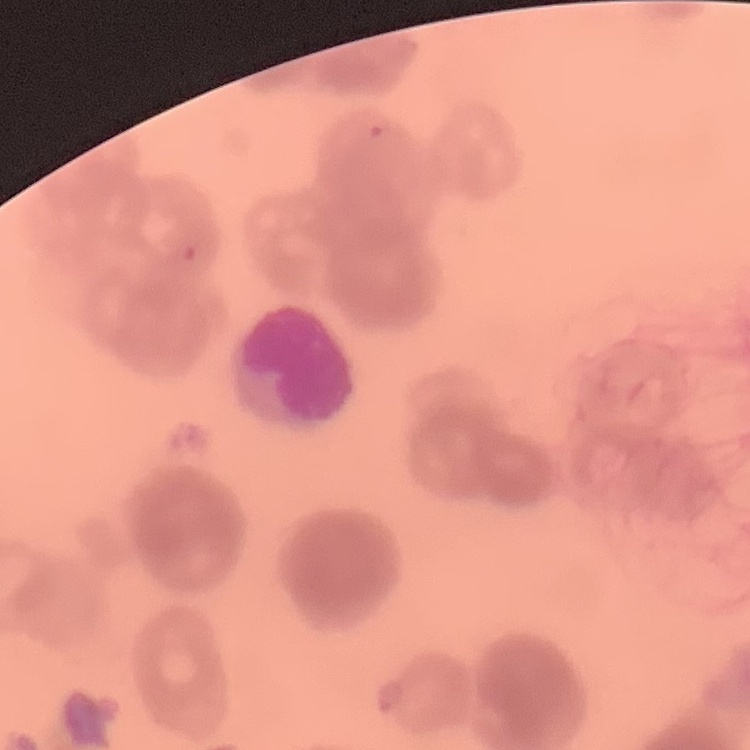

The erythrocytes show rouleaux formation. Stained with either Field's or Giemsa. Thin peripheral smear. One tile cut from a larger photomicrograph.